Locate and identify every blood parasite.
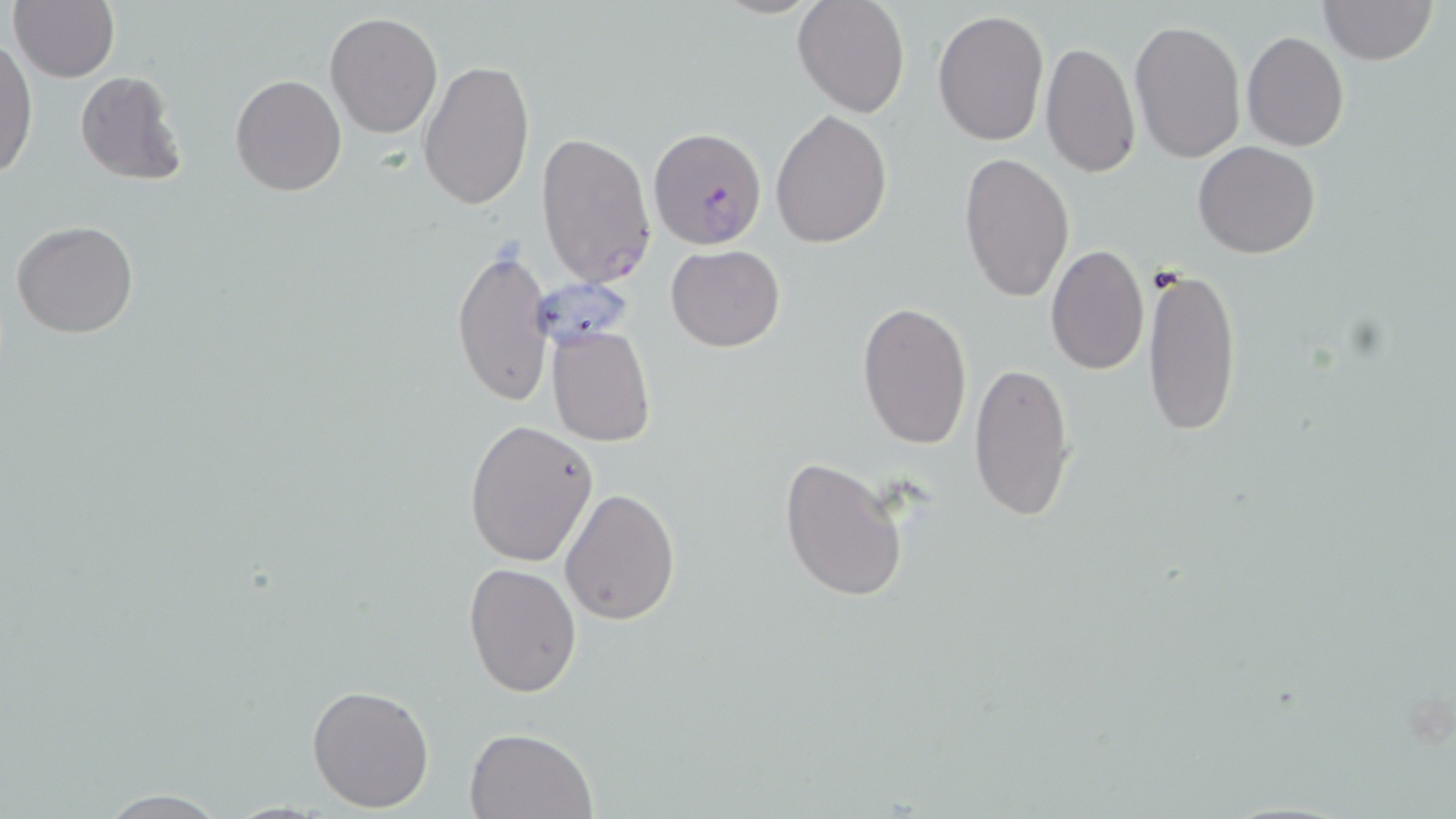
Approximate bounding boxes as (x1,y1)-(x2,y2) corner pairs in pixels.
Plasmodium falciparum-infected red blood cells: (647,126)-(769,249).
No Plasmodium ovale, Plasmodium malariae, Plasmodium vivax, Babesia divergens, or Trypanosoma brucei observed.

Summary:
  - Uninfected red blood cell locations: (10,0)-(119,82), (792,0)-(910,118), (1318,0)-(1438,66), (933,9)-(1049,145), (325,11)-(444,139), (1130,19)-(1246,164), (1241,31)-(1350,151), (0,38)-(37,179), (1039,39)-(1140,180), (418,58)-(536,212), (75,71)-(187,187), (231,73)-(346,195), (771,109)-(892,249), (535,131)-(657,288), (1194,140)-(1321,258), (958,152)-(1072,303), (11,219)-(138,338), (1046,243)-(1148,377), (665,244)-(784,351), (451,246)-(553,408), (1142,267)-(1242,437), (857,302)-(972,450), (546,326)-(657,447), (970,360)-(1077,523), (466,419)-(597,565), (779,456)-(909,602), (561,488)-(678,625), (462,562)-(583,699), (306,682)-(436,813), (464,727)-(597,818), (89,789)-(237,818)
  - Slide-level diagnosis: Plasmodium falciparum
  - Stain: May-Grünwald-Giemsa
  - Image size: 1456×819 pixels
  - Preparation: thin blood smear
  - Magnification: 1000x
  - Field of view: one of a larger specimen
  - Modality: optical microscopy